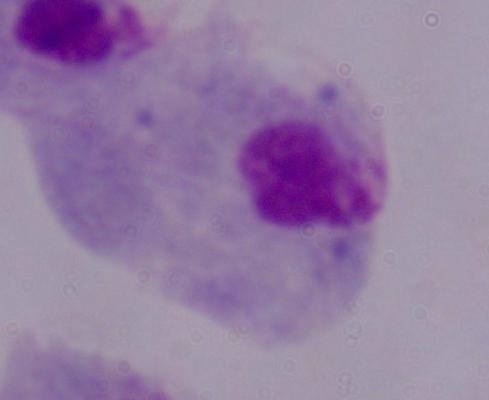
Summary:
  - Modality: photomicrograph
  - Identification: trichomonad
  - Magnification: 1000x